Point out each Plasmodium parasite.
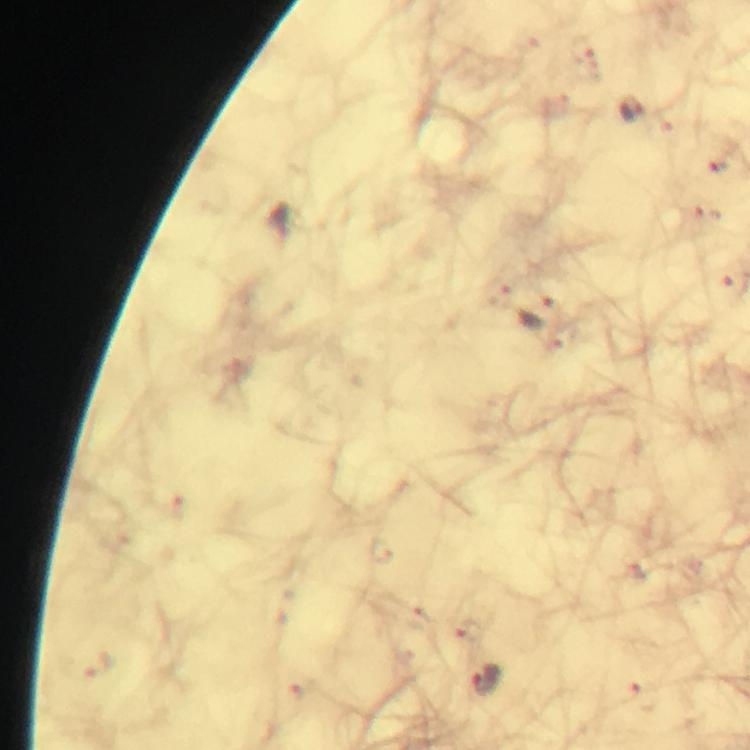
Approximate centers as {x, y} in pixels.
Plasmodium parasites: {631, 108}, {540, 311}, {487, 680}, {640, 696}.

A crop from one field of view. Giemsa-stained preparation. Immersion oil was used. Image is 750×750 pixels. From a diagnostic examination for malaria. Thick smear. 100x magnification. Smartphone photograph taken through a microscope.